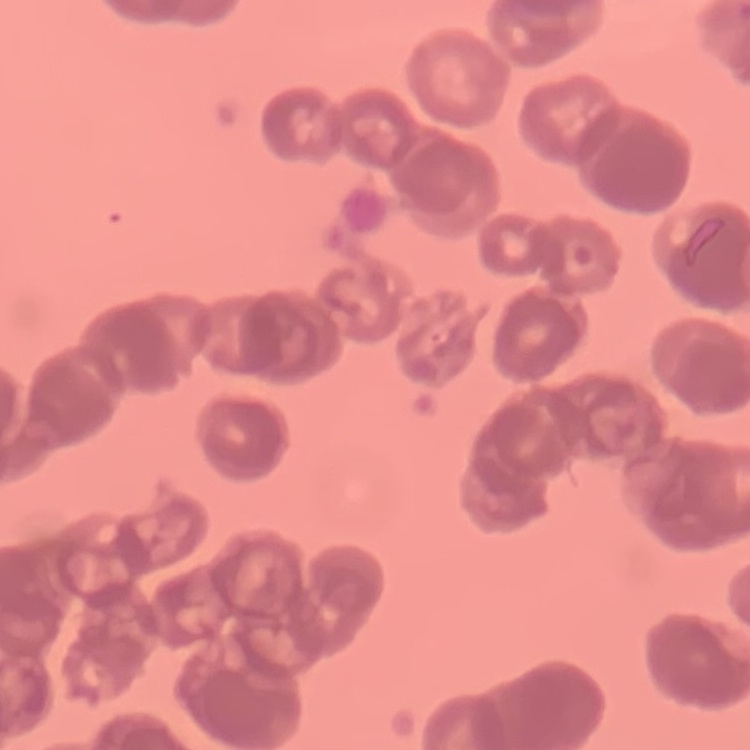
Summary:
  - Red blood cell morphology: rouleaux formation
  - Stain: Field's or Giemsa
  - Image type: square crop of a larger photomicrograph
  - Preparation: thin peripheral smear